Give the extent of all uninfected red blood cells.
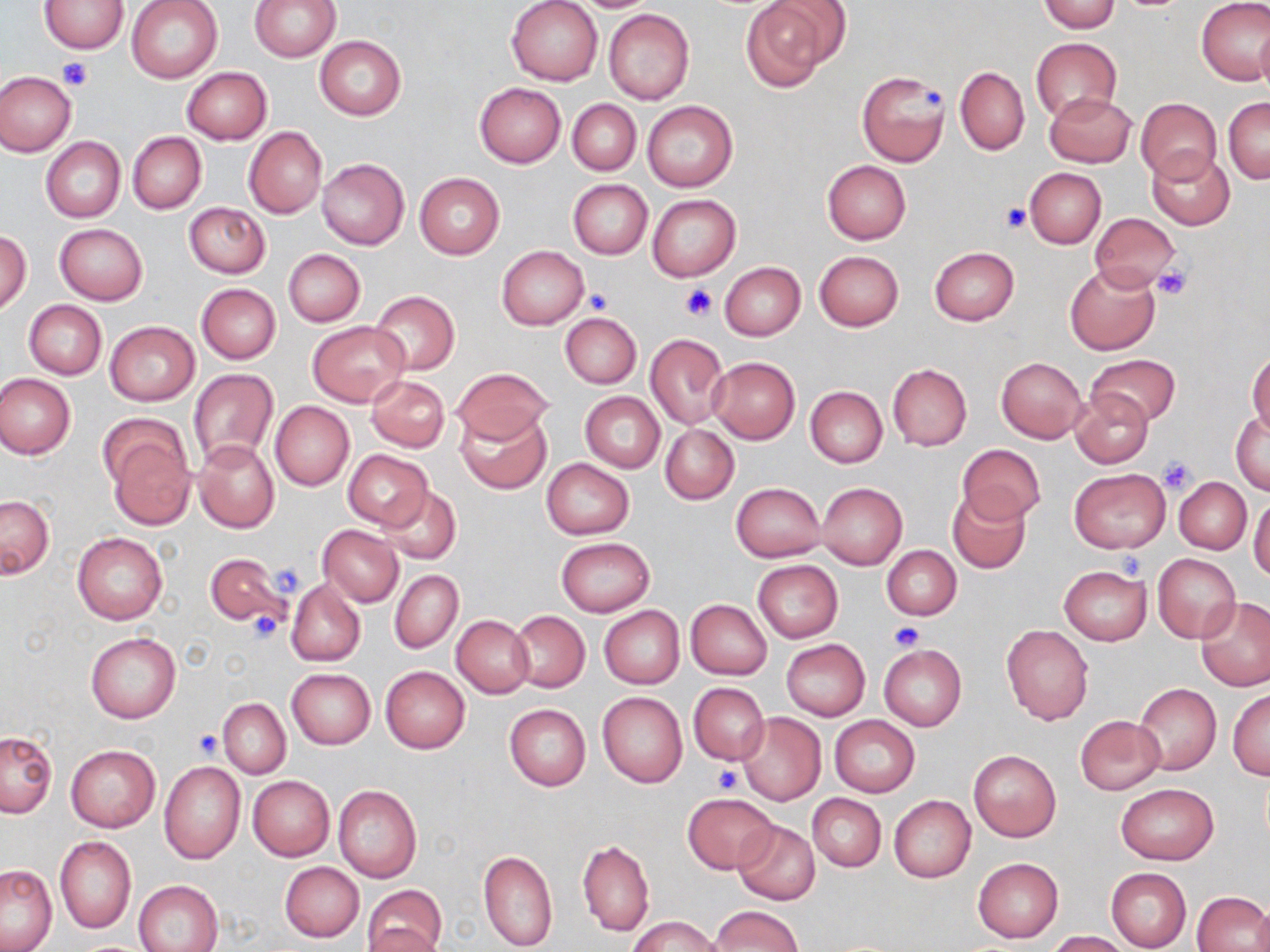

Approximate bounding boxes as (x1,y1)-(x2,y2) corner pairs in pixels.
Uninfected red blood cells: (38,0)-(129,53), (125,0)-(224,83), (250,0)-(340,62), (506,0)-(603,86), (742,0)-(848,90), (1040,0)-(1120,33), (1197,0)-(1270,85), (603,9)-(695,105), (1255,23)-(1270,100), (314,35)-(407,120), (1031,38)-(1122,121), (955,66)-(1029,156), (181,67)-(272,145), (0,70)-(76,157), (857,70)-(949,167), (474,83)-(566,167), (1044,92)-(1136,167), (1136,97)-(1222,184), (1223,98)-(1270,183), (568,99)-(640,175), (643,100)-(739,192), (244,126)-(327,218), (128,132)-(206,214), (40,137)-(125,223), (1147,149)-(1234,229), (317,158)-(409,249), (822,160)-(911,244), (1024,167)-(1106,248), (414,173)-(504,259), (568,180)-(651,259), (647,195)-(739,280), (184,202)-(270,279), (1089,213)-(1181,291), (53,223)-(148,305), (0,231)-(31,315), (497,245)-(588,329), (929,246)-(1019,325), (283,249)-(365,326), (814,250)-(904,332), (720,261)-(805,341), (1064,264)-(1160,355), (195,283)-(281,363), (371,290)-(459,375), (24,300)-(106,379), (561,312)-(641,387), (105,321)-(201,406), (307,321)-(409,406), (645,333)-(728,429), (1247,349)-(1269,436), (1087,353)-(1180,427), (708,356)-(800,443), (996,357)-(1086,442), (887,364)-(971,451), (450,366)-(555,446), (188,368)-(279,467), (0,373)-(75,458), (366,374)-(450,452), (806,386)-(887,468), (1070,390)-(1154,467), (580,392)-(664,473), (270,401)-(354,492), (1231,408)-(1269,495), (456,409)-(552,494), (660,424)-(738,504), (104,428)-(197,529), (192,439)-(279,533), (957,442)-(1044,525), (343,450)-(432,530), (542,458)-(635,540), (1069,468)-(1169,553), (1174,476)-(1251,555), (731,482)-(826,562), (818,482)-(907,569), (376,485)-(460,566), (948,491)-(1031,574), (1249,491)-(1270,581), (1,496)-(53,578), (318,525)-(404,606), (72,531)-(168,625), (557,536)-(654,617), (882,545)-(960,621), (205,551)-(288,626), (1152,553)-(1241,642), (753,560)-(842,642), (1059,565)-(1152,644), (389,570)-(463,654), (286,579)-(366,667), (1197,597)-(1270,691), (686,598)-(772,680), (599,605)-(684,689), (510,610)-(589,693), (452,615)-(534,697), (1002,624)-(1094,725), (85,631)-(181,724), (782,640)-(870,720), (878,645)-(966,731), (380,666)-(470,753), (286,669)-(375,749), (687,683)-(770,765), (1134,684)-(1221,774), (1228,688)-(1269,780), (597,691)-(687,788), (218,698)-(290,778), (504,704)-(590,792), (737,712)-(826,805), (830,715)-(920,797), (1075,715)-(1164,794), (0,731)-(57,817), (66,744)-(160,832), (969,750)-(1061,842), (160,762)-(245,863), (247,775)-(335,861), (1115,783)-(1218,864), (333,785)-(422,883), (682,793)-(778,874), (807,793)-(886,871), (889,795)-(975,883), (731,820)-(820,905), (55,836)-(136,934), (577,840)-(654,936), (478,850)-(558,950), (973,857)-(1064,943), (279,861)-(364,942), (1,864)-(58,952), (1106,867)-(1191,951), (134,879)-(223,952), (362,883)-(447,952), (1192,890)-(1269,951), (1251,902)-(1270,951), (708,905)-(802,951), (629,916)-(719,952), (363,925)-(443,952), (1044,930)-(1130,951).

Summary:
  - Platelet locations: (59,58)-(93,91), (921,87)-(946,114), (1001,203)-(1030,232), (1151,264)-(1193,301), (679,285)-(718,323), (585,288)-(613,315), (1159,455)-(1198,495), (1118,552)-(1145,583), (266,562)-(307,598), (246,609)-(283,644), (889,620)-(926,653), (192,729)-(224,760), (712,765)-(740,794)
  - Slide-level diagnosis: no evidence of blood parasites
  - Modality: light microscopy
  - Image size: 1270×952 pixels
  - Magnification: 1000x
  - Field of view: single
  - Stain: May-Grünwald-Giemsa
  - Preparation: thin blood film